Give the extent of all Plasmodium falciparum-infected red blood cells.
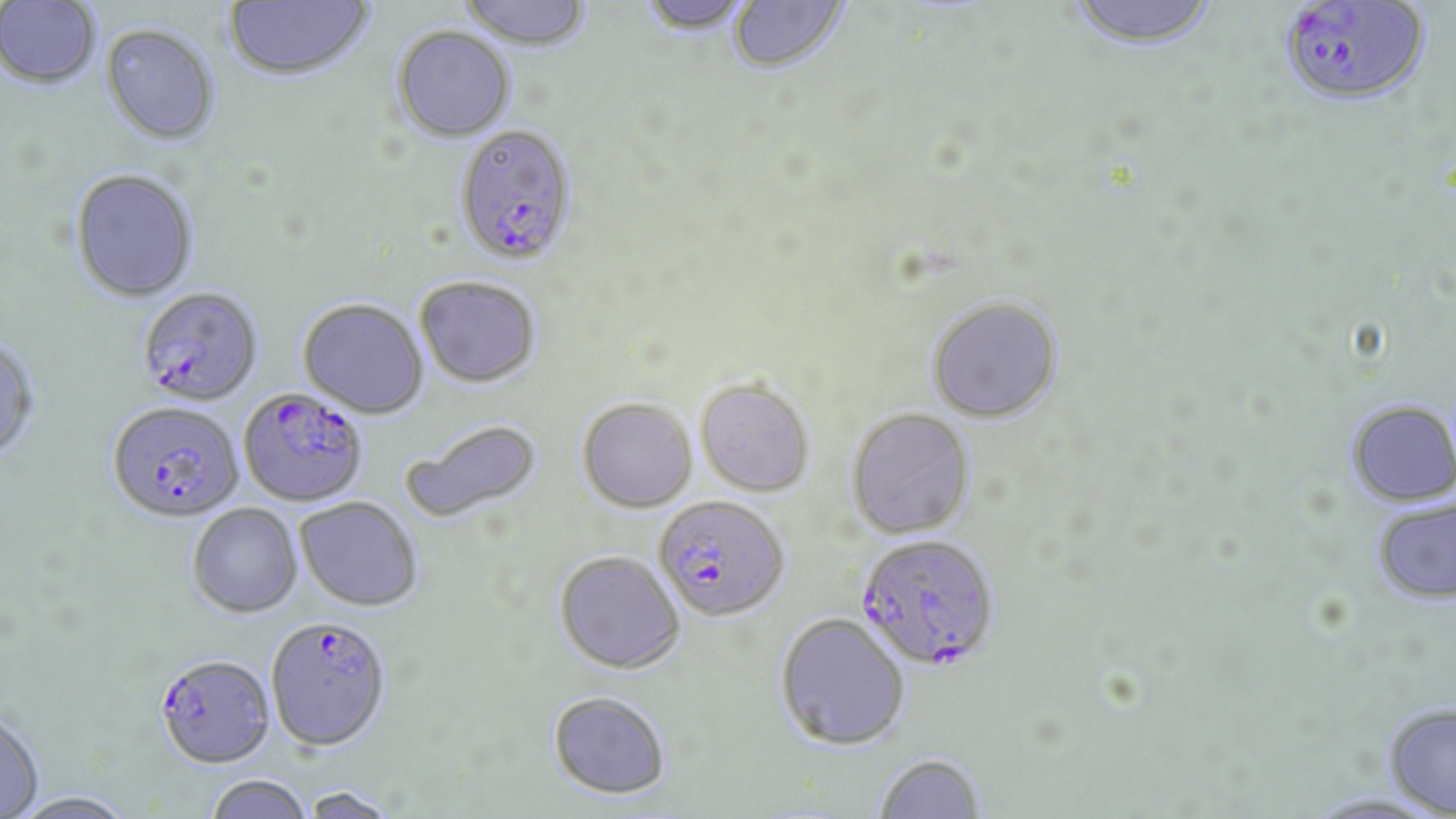
Approximate bounding boxes as (x1, y1, x2, y2) in pixels.
Plasmodium falciparum-infected red blood cells: (1276, 2, 1431, 107), (459, 129, 584, 272), (137, 287, 263, 407), (239, 387, 368, 507), (108, 401, 243, 523), (654, 496, 790, 621), (855, 531, 1001, 671), (267, 613, 387, 754), (155, 653, 275, 768).

{
  "slide_level_diagnosis": "Plasmodium falciparum",
  "magnification": "1000x",
  "field_of_view": "single",
  "stain": "May-Grünwald-Giemsa",
  "image_size": "1456×819 pixels",
  "uninfected_red_blood_cell_locations": "approximate bounding boxes as (x1, y1, x2, y2) in pixels: (224, 0, 375, 83), (458, 0, 594, 52), (636, 0, 753, 35), (728, 0, 849, 74), (1063, 0, 1221, 50), (0, 1, 101, 90), (101, 24, 221, 145), (392, 25, 516, 142), (70, 169, 200, 303), (414, 275, 541, 387), (926, 296, 1063, 424), (298, 297, 429, 418), (0, 336, 41, 463), (695, 377, 815, 497), (577, 397, 697, 512), (1346, 399, 1456, 507), (847, 407, 976, 539), (401, 419, 543, 526), (295, 497, 423, 611), (1372, 497, 1456, 604), (188, 504, 302, 617), (554, 550, 685, 673), (775, 613, 910, 750), (547, 690, 671, 798), (1384, 702, 1456, 815), (0, 709, 45, 817), (872, 752, 987, 818), (205, 775, 313, 819), (300, 786, 401, 818), (12, 791, 135, 819)",
  "modality": "optical microscopy",
  "preparation": "thin blood smear"
}